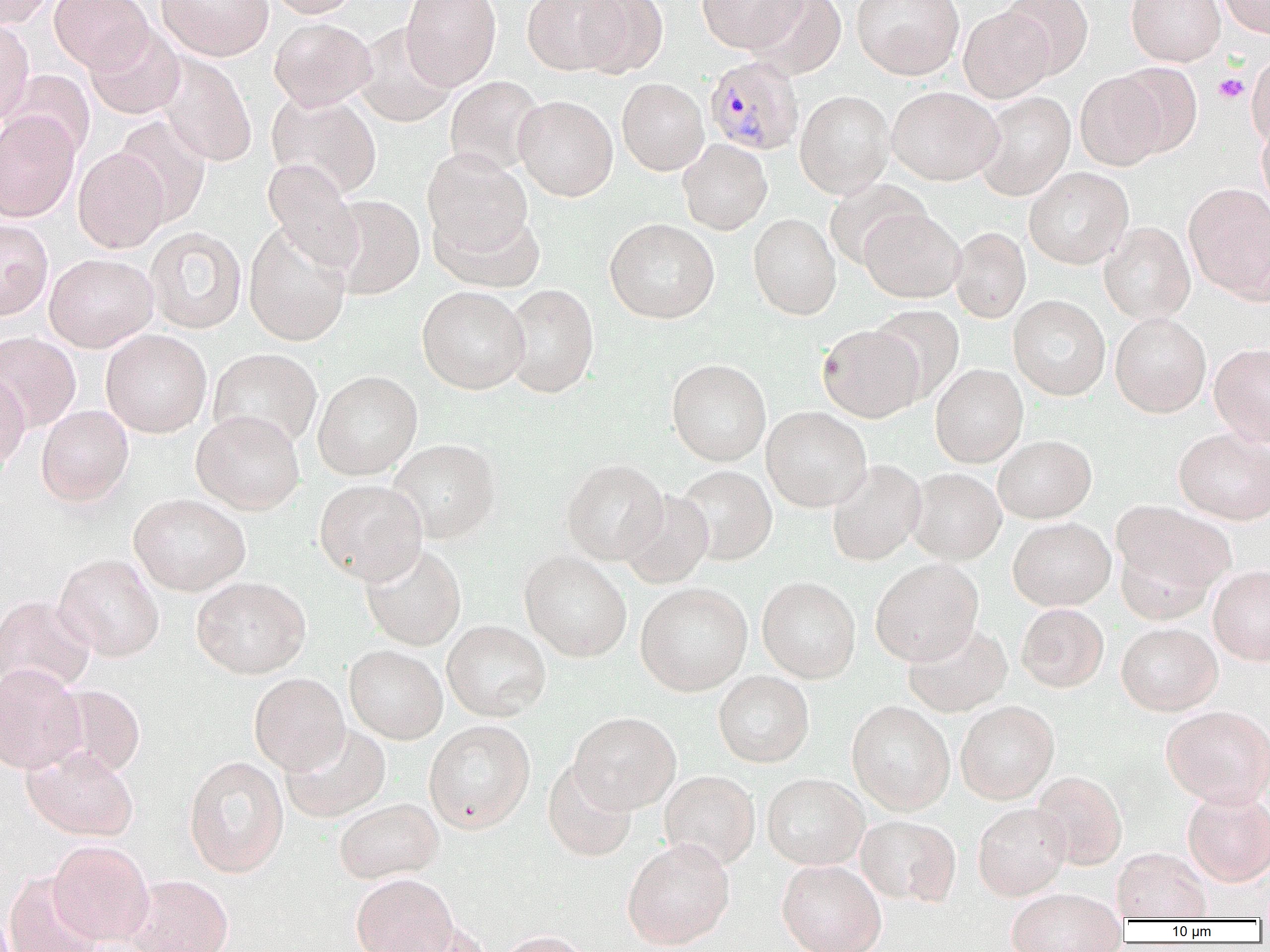

Plasmodium malariae-infected red blood cell locations = approximate bounding boxes as (x1, y1, x2, y2) in pixels: (704, 55, 804, 155)
slide-level diagnosis = Plasmodium malariae
field of view = single
platelet locations = approximate bounding boxes as (x1, y1, x2, y2) in pixels: (1214, 73, 1249, 103)
magnification = 1000x
preparation = thin blood film
modality = optical microscopy
image size = 1270×952 pixels
uninfected red blood cell locations = approximate bounding boxes as (x1, y1, x2, y2) in pixels: (0, 0, 54, 28), (49, 0, 152, 72), (155, 0, 274, 61), (266, 0, 360, 18), (401, 0, 502, 90), (521, 0, 629, 75), (575, 0, 668, 78), (696, 0, 807, 54), (747, 0, 847, 80), (851, 0, 964, 80), (1000, 0, 1094, 79), (1126, 0, 1225, 66), (1218, 0, 1270, 39), (958, 6, 1054, 103), (0, 18, 34, 124), (269, 18, 376, 110), (84, 23, 185, 120), (353, 24, 456, 127), (1246, 52, 1270, 149), (154, 53, 257, 167), (1110, 63, 1202, 159), (2, 70, 95, 161), (1074, 70, 1170, 170), (445, 76, 546, 176), (617, 78, 709, 175), (887, 86, 1003, 185), (795, 90, 894, 199), (266, 92, 382, 198), (974, 92, 1075, 200), (514, 95, 618, 202), (0, 112, 80, 223), (113, 114, 211, 227), (1256, 122, 1270, 214), (678, 139, 772, 235), (73, 147, 169, 254), (423, 148, 533, 257), (261, 158, 363, 272), (1024, 167, 1133, 269), (823, 178, 930, 271), (1183, 183, 1270, 301), (327, 194, 425, 300), (431, 208, 545, 294), (859, 208, 966, 303), (748, 213, 841, 320), (605, 218, 720, 324), (0, 219, 53, 320), (243, 221, 352, 347), (1099, 222, 1195, 325), (144, 226, 247, 334), (949, 226, 1031, 323), (44, 253, 158, 352), (501, 283, 599, 398), (417, 286, 530, 394), (1008, 295, 1110, 400), (870, 305, 964, 403), (1110, 312, 1211, 417), (817, 324, 925, 423), (100, 329, 211, 438), (0, 332, 81, 432), (1209, 344, 1270, 447), (207, 348, 323, 451), (666, 359, 771, 466), (930, 364, 1028, 467), (0, 370, 31, 471), (313, 370, 423, 481), (36, 405, 134, 507), (761, 406, 872, 512), (191, 410, 305, 514), (1173, 429, 1270, 525), (993, 435, 1097, 523), (388, 439, 501, 543), (561, 458, 668, 565), (826, 459, 927, 567), (675, 465, 777, 565), (908, 468, 1006, 564), (314, 478, 427, 584), (616, 490, 715, 588), (128, 493, 250, 595), (1111, 500, 1235, 607), (1008, 517, 1116, 611), (360, 542, 466, 650), (519, 551, 632, 662), (53, 553, 165, 662), (871, 559, 983, 666), (1208, 565, 1270, 666), (191, 576, 310, 678), (757, 576, 861, 683), (635, 582, 753, 696), (0, 595, 96, 694), (1016, 603, 1109, 692), (442, 620, 551, 721), (902, 622, 1013, 718), (1116, 622, 1223, 715), (344, 645, 448, 744), (0, 663, 87, 775), (713, 671, 814, 768), (249, 673, 349, 775), (53, 685, 145, 777), (846, 701, 955, 816), (956, 701, 1060, 804), (1160, 705, 1270, 808), (569, 712, 681, 814), (423, 720, 535, 833), (279, 723, 391, 823), (22, 745, 138, 841), (183, 756, 289, 878), (542, 760, 638, 862), (659, 771, 760, 870), (1031, 772, 1127, 870), (762, 774, 869, 871), (1182, 790, 1270, 887), (333, 797, 444, 883), (973, 803, 1071, 900), (855, 816, 961, 908), (48, 839, 154, 946), (622, 839, 736, 950), (1111, 848, 1211, 922), (777, 860, 886, 952), (3, 870, 104, 952), (351, 873, 457, 952), (126, 874, 233, 952), (1005, 889, 1127, 952), (394, 922, 493, 952), (496, 930, 594, 952)